Report the malaria status of this cell.
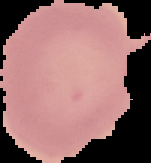

It is uninfected.

Summary:
  - Image type: segmented cell region on a black background
  - Image size: 151×163 pixels
  - Preparation: thin blood film